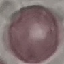 Result: negative for malaria parasites. Photographed with a smartphone camera at the microscope eyepiece. Automatically extracted cell patch, resized to 64 × 64 pixels. Thin smear of blood. Giemsa stain.